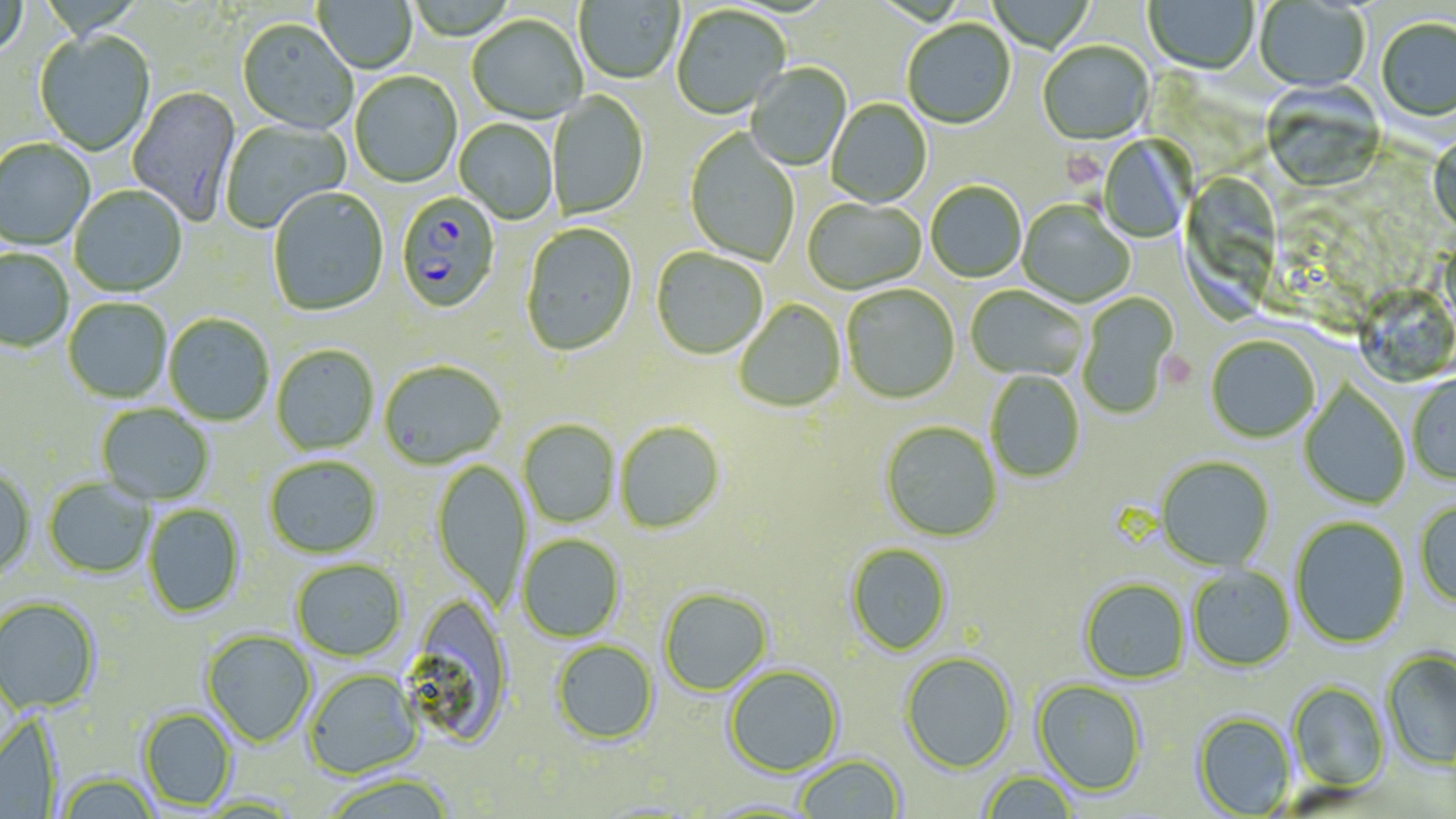
{
  "slide_level_diagnosis": "Plasmodium falciparum",
  "stain": "May-Grünwald-Giemsa",
  "field_of_view": "single",
  "modality": "optical microscopy",
  "preparation": "thin blood smear",
  "platelet_locations": "approximate bounding boxes as (x1,y1)-(x2,y2) corner pairs in pixels: (1063,149)-(1102,186), (1158,349)-(1197,391)",
  "image_size": "1456×819 pixels",
  "magnification": "1000x",
  "plasmodium_falciparum_infected_red_blood_cell_locations": "approximate bounding boxes as (x1,y1)-(x2,y2) corner pairs in pixels: (395,192)-(501,316)",
  "uninfected_red_blood_cell_locations": "approximate bounding boxes as (x1,y1)-(x2,y2) corner pairs in pixels: (0,0)-(28,64), (313,0)-(417,74), (574,0)-(685,86), (988,0)-(1096,53), (1144,0)-(1259,76), (1254,1)-(1370,93), (671,7)-(791,120), (467,16)-(587,125), (1376,19)-(1456,125), (236,21)-(358,137), (902,21)-(1016,130), (35,31)-(156,157), (1037,43)-(1154,146), (745,64)-(852,171), (349,73)-(462,189), (1260,83)-(1386,194), (126,86)-(242,226), (548,92)-(649,220), (826,99)-(932,208), (220,118)-(351,234), (454,119)-(558,225), (684,129)-(799,267), (1429,133)-(1456,236), (1099,136)-(1193,243), (0,139)-(95,251), (1182,171)-(1279,329), (926,182)-(1027,283), (69,186)-(187,298), (267,188)-(389,317), (803,198)-(926,295), (1017,202)-(1135,308), (521,223)-(638,357), (651,248)-(769,360), (0,249)-(73,353), (1351,283)-(1453,381), (842,285)-(960,404), (965,285)-(1089,382), (1078,292)-(1178,420), (63,298)-(172,403), (735,299)-(846,412), (164,314)-(274,426), (1206,335)-(1320,443), (272,345)-(379,455), (379,361)-(507,471), (985,370)-(1085,483), (1407,375)-(1456,486), (1298,382)-(1411,510), (97,404)-(214,505), (518,420)-(620,528), (615,421)-(725,534), (880,421)-(1002,542), (264,455)-(383,559), (1155,456)-(1275,571), (431,459)-(532,611), (0,466)-(35,578), (43,478)-(154,579), (1414,501)-(1456,610), (142,504)-(245,618), (1290,516)-(1410,649), (517,534)-(625,642), (845,543)-(952,656), (291,558)-(407,661), (1187,566)-(1296,672), (1079,577)-(1191,684), (659,587)-(772,697), (0,597)-(101,714), (399,599)-(515,748), (201,629)-(317,747), (551,640)-(659,745), (1382,649)-(1456,769), (899,652)-(1017,773), (723,664)-(844,777), (303,669)-(424,779), (1032,679)-(1148,797), (1287,681)-(1390,791), (139,708)-(236,810), (1192,711)-(1296,817), (0,714)-(63,818), (794,754)-(906,818), (978,770)-(1079,818), (319,773)-(459,819), (58,774)-(160,819), (696,797)-(824,818)"
}